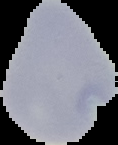
preparation = thin blood film
image size = 118×145 pixels
malaria status = uninfected
image type = segmented cell region with the area outside set to black